Assess this cell for malaria.
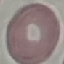

It is uninfected.

Giemsa-stained preparation. Thin smear of blood. Acquired by smartphone through the microscope eyepiece. Cell patch, automatically extracted from a larger field of view and resized to 64 × 64 pixels.